Name the blood parasite species.
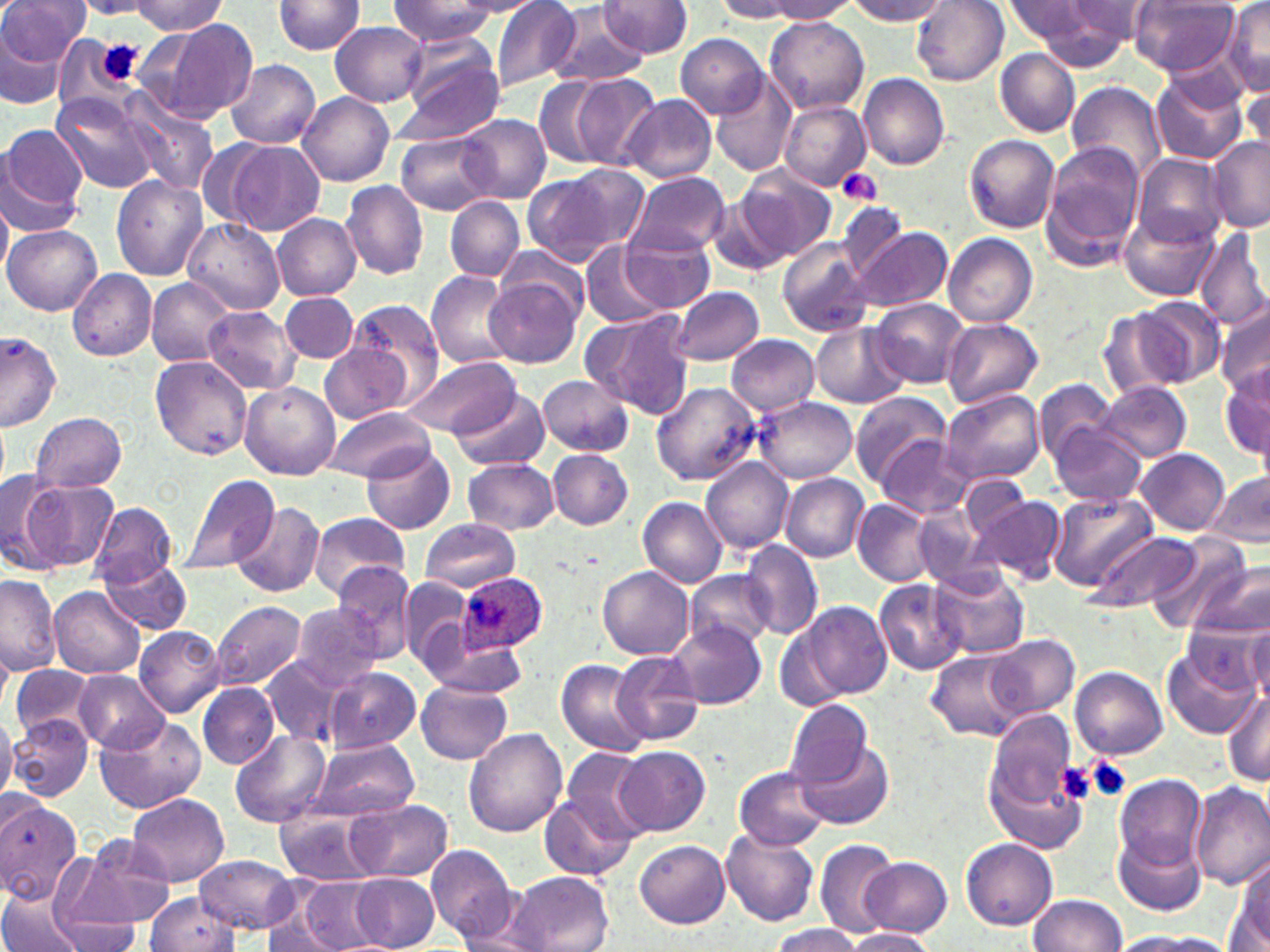
Plasmodium ovale.

Approximate bounding boxes as named x1/y1/x2/y2 corners in pixels. Platelet locations: (x1=96, y1=40, x2=144, y2=86), (x1=837, y1=168, x2=884, y2=206), (x1=1082, y1=755, x2=1131, y2=803), (x1=1053, y1=761, x2=1096, y2=805). Uninfected red blood cell locations: (x1=1, y1=0, x2=85, y2=72), (x1=390, y1=0, x2=500, y2=47), (x1=455, y1=0, x2=540, y2=15), (x1=490, y1=0, x2=582, y2=94), (x1=766, y1=0, x2=859, y2=20), (x1=846, y1=0, x2=951, y2=24), (x1=1004, y1=0, x2=1096, y2=45), (x1=127, y1=1, x2=228, y2=34), (x1=271, y1=1, x2=367, y2=56), (x1=600, y1=1, x2=692, y2=58), (x1=715, y1=1, x2=802, y2=22), (x1=912, y1=1, x2=1009, y2=87), (x1=1071, y1=1, x2=1161, y2=44), (x1=1129, y1=1, x2=1239, y2=76), (x1=1020, y1=2, x2=1137, y2=68), (x1=1221, y1=2, x2=1270, y2=96), (x1=550, y1=6, x2=648, y2=87), (x1=764, y1=15, x2=870, y2=114), (x1=150, y1=18, x2=257, y2=125), (x1=330, y1=21, x2=428, y2=107), (x1=0, y1=26, x2=70, y2=110), (x1=677, y1=35, x2=767, y2=116), (x1=393, y1=36, x2=506, y2=143), (x1=994, y1=46, x2=1081, y2=137), (x1=226, y1=60, x2=321, y2=148), (x1=1151, y1=72, x2=1247, y2=164), (x1=858, y1=73, x2=949, y2=170), (x1=571, y1=75, x2=661, y2=168), (x1=712, y1=76, x2=797, y2=177), (x1=535, y1=77, x2=611, y2=167), (x1=1240, y1=81, x2=1270, y2=157), (x1=1067, y1=82, x2=1168, y2=182), (x1=298, y1=91, x2=395, y2=185), (x1=51, y1=92, x2=161, y2=194), (x1=622, y1=94, x2=718, y2=184), (x1=118, y1=95, x2=219, y2=194), (x1=780, y1=100, x2=870, y2=191), (x1=457, y1=113, x2=550, y2=203), (x1=0, y1=123, x2=89, y2=233), (x1=396, y1=131, x2=495, y2=215), (x1=963, y1=134, x2=1060, y2=232), (x1=1206, y1=136, x2=1269, y2=231), (x1=198, y1=138, x2=275, y2=229), (x1=223, y1=141, x2=325, y2=236), (x1=1041, y1=142, x2=1145, y2=269), (x1=1131, y1=152, x2=1228, y2=246), (x1=562, y1=162, x2=651, y2=254), (x1=736, y1=165, x2=835, y2=261), (x1=627, y1=172, x2=730, y2=256), (x1=112, y1=173, x2=209, y2=280), (x1=522, y1=173, x2=616, y2=266), (x1=342, y1=181, x2=430, y2=280), (x1=705, y1=193, x2=794, y2=277), (x1=444, y1=196, x2=524, y2=281), (x1=0, y1=200, x2=12, y2=282), (x1=833, y1=200, x2=910, y2=280), (x1=1119, y1=206, x2=1220, y2=303), (x1=273, y1=214, x2=363, y2=300), (x1=183, y1=219, x2=284, y2=312), (x1=3, y1=224, x2=102, y2=315), (x1=848, y1=224, x2=953, y2=313), (x1=1195, y1=226, x2=1270, y2=332), (x1=621, y1=231, x2=716, y2=312), (x1=943, y1=234, x2=1038, y2=327), (x1=774, y1=237, x2=876, y2=340), (x1=581, y1=243, x2=669, y2=328), (x1=496, y1=244, x2=592, y2=324), (x1=67, y1=269, x2=157, y2=360), (x1=426, y1=270, x2=517, y2=368), (x1=485, y1=274, x2=583, y2=368), (x1=146, y1=277, x2=238, y2=368), (x1=669, y1=285, x2=765, y2=366), (x1=280, y1=293, x2=359, y2=362), (x1=870, y1=297, x2=969, y2=388), (x1=1131, y1=297, x2=1224, y2=388), (x1=348, y1=300, x2=445, y2=403), (x1=1098, y1=306, x2=1191, y2=399), (x1=203, y1=307, x2=300, y2=394), (x1=1217, y1=307, x2=1270, y2=398), (x1=582, y1=309, x2=696, y2=420), (x1=333, y1=312, x2=480, y2=438), (x1=942, y1=319, x2=1042, y2=411), (x1=812, y1=322, x2=906, y2=408), (x1=0, y1=332, x2=62, y2=433), (x1=726, y1=334, x2=820, y2=415), (x1=318, y1=342, x2=414, y2=424), (x1=151, y1=355, x2=252, y2=458), (x1=405, y1=355, x2=518, y2=438), (x1=1220, y1=367, x2=1270, y2=461), (x1=537, y1=374, x2=634, y2=457), (x1=1035, y1=378, x2=1119, y2=465), (x1=1098, y1=380, x2=1191, y2=462), (x1=651, y1=381, x2=763, y2=486), (x1=239, y1=382, x2=339, y2=481), (x1=452, y1=388, x2=550, y2=472), (x1=941, y1=388, x2=1045, y2=486), (x1=849, y1=389, x2=951, y2=489), (x1=752, y1=397, x2=857, y2=484), (x1=320, y1=408, x2=437, y2=481), (x1=31, y1=411, x2=126, y2=493), (x1=1049, y1=421, x2=1147, y2=505), (x1=877, y1=436, x2=973, y2=519), (x1=363, y1=441, x2=454, y2=533), (x1=1137, y1=448, x2=1230, y2=535), (x1=548, y1=450, x2=633, y2=530), (x1=462, y1=458, x2=559, y2=535), (x1=700, y1=458, x2=794, y2=554), (x1=0, y1=468, x2=63, y2=572), (x1=959, y1=472, x2=1032, y2=544), (x1=1207, y1=472, x2=1270, y2=550), (x1=175, y1=473, x2=280, y2=576), (x1=779, y1=474, x2=870, y2=562), (x1=19, y1=479, x2=117, y2=573), (x1=1048, y1=491, x2=1158, y2=592), (x1=971, y1=494, x2=1066, y2=588), (x1=637, y1=497, x2=728, y2=588), (x1=231, y1=500, x2=325, y2=598), (x1=854, y1=500, x2=940, y2=586), (x1=912, y1=502, x2=991, y2=587), (x1=90, y1=503, x2=177, y2=587), (x1=308, y1=512, x2=409, y2=600), (x1=421, y1=518, x2=519, y2=592), (x1=1084, y1=529, x2=1200, y2=614), (x1=1148, y1=535, x2=1253, y2=634), (x1=740, y1=540, x2=823, y2=639), (x1=100, y1=557, x2=192, y2=635), (x1=1191, y1=558, x2=1270, y2=644), (x1=335, y1=563, x2=417, y2=659), (x1=930, y1=565, x2=1028, y2=660), (x1=598, y1=566, x2=693, y2=659), (x1=684, y1=570, x2=775, y2=652), (x1=0, y1=574, x2=61, y2=677), (x1=397, y1=577, x2=474, y2=673), (x1=875, y1=579, x2=968, y2=675), (x1=49, y1=587, x2=145, y2=678), (x1=212, y1=599, x2=309, y2=692), (x1=790, y1=599, x2=893, y2=705), (x1=290, y1=602, x2=383, y2=691), (x1=1244, y1=618, x2=1270, y2=711), (x1=669, y1=622, x2=765, y2=709), (x1=135, y1=626, x2=226, y2=718), (x1=986, y1=633, x2=1079, y2=720), (x1=429, y1=639, x2=531, y2=694), (x1=1162, y1=642, x2=1258, y2=737), (x1=613, y1=650, x2=704, y2=748), (x1=927, y1=650, x2=1024, y2=741), (x1=261, y1=657, x2=343, y2=745), (x1=555, y1=657, x2=651, y2=756), (x1=11, y1=666, x2=99, y2=742), (x1=324, y1=666, x2=420, y2=754), (x1=1072, y1=666, x2=1167, y2=759), (x1=74, y1=669, x2=170, y2=754), (x1=417, y1=679, x2=513, y2=764), (x1=198, y1=683, x2=278, y2=767), (x1=1222, y1=688, x2=1270, y2=788), (x1=784, y1=699, x2=873, y2=787), (x1=0, y1=710, x2=17, y2=806), (x1=8, y1=713, x2=94, y2=801), (x1=94, y1=714, x2=206, y2=813), (x1=987, y1=716, x2=1086, y2=856), (x1=463, y1=729, x2=567, y2=837), (x1=231, y1=730, x2=331, y2=827), (x1=311, y1=738, x2=417, y2=820), (x1=798, y1=741, x2=895, y2=829), (x1=560, y1=744, x2=655, y2=846), (x1=615, y1=745, x2=709, y2=834), (x1=735, y1=769, x2=829, y2=849), (x1=1115, y1=774, x2=1211, y2=875), (x1=1191, y1=782, x2=1270, y2=889), (x1=127, y1=792, x2=229, y2=887), (x1=539, y1=792, x2=637, y2=883), (x1=347, y1=798, x2=452, y2=883), (x1=1, y1=799, x2=83, y2=905), (x1=274, y1=805, x2=383, y2=885), (x1=722, y1=827, x2=822, y2=927), (x1=1115, y1=832, x2=1207, y2=917), (x1=62, y1=833, x2=178, y2=933), (x1=813, y1=838, x2=897, y2=934), (x1=961, y1=838, x2=1057, y2=929), (x1=635, y1=840, x2=731, y2=928), (x1=426, y1=844, x2=518, y2=942), (x1=195, y1=854, x2=299, y2=934), (x1=1233, y1=855, x2=1269, y2=946), (x1=860, y1=856, x2=952, y2=937), (x1=510, y1=870, x2=613, y2=951), (x1=350, y1=872, x2=439, y2=952), (x1=295, y1=876, x2=384, y2=952), (x1=0, y1=885, x2=86, y2=952), (x1=144, y1=893, x2=239, y2=951), (x1=1028, y1=894, x2=1127, y2=952), (x1=53, y1=914, x2=142, y2=951), (x1=453, y1=914, x2=552, y2=952), (x1=263, y1=923, x2=342, y2=951), (x1=769, y1=925, x2=864, y2=952), (x1=844, y1=927, x2=938, y2=951), (x1=1110, y1=931, x2=1226, y2=951). Plasmodium ovale-infected red blood cell locations: (x1=457, y1=573, x2=550, y2=656). May-Grünwald-Giemsa stain. One field of a larger specimen. 1000x magnification. Thin blood film. Image is 1270×952 pixels. Optical microscopy.